State the preparation type.
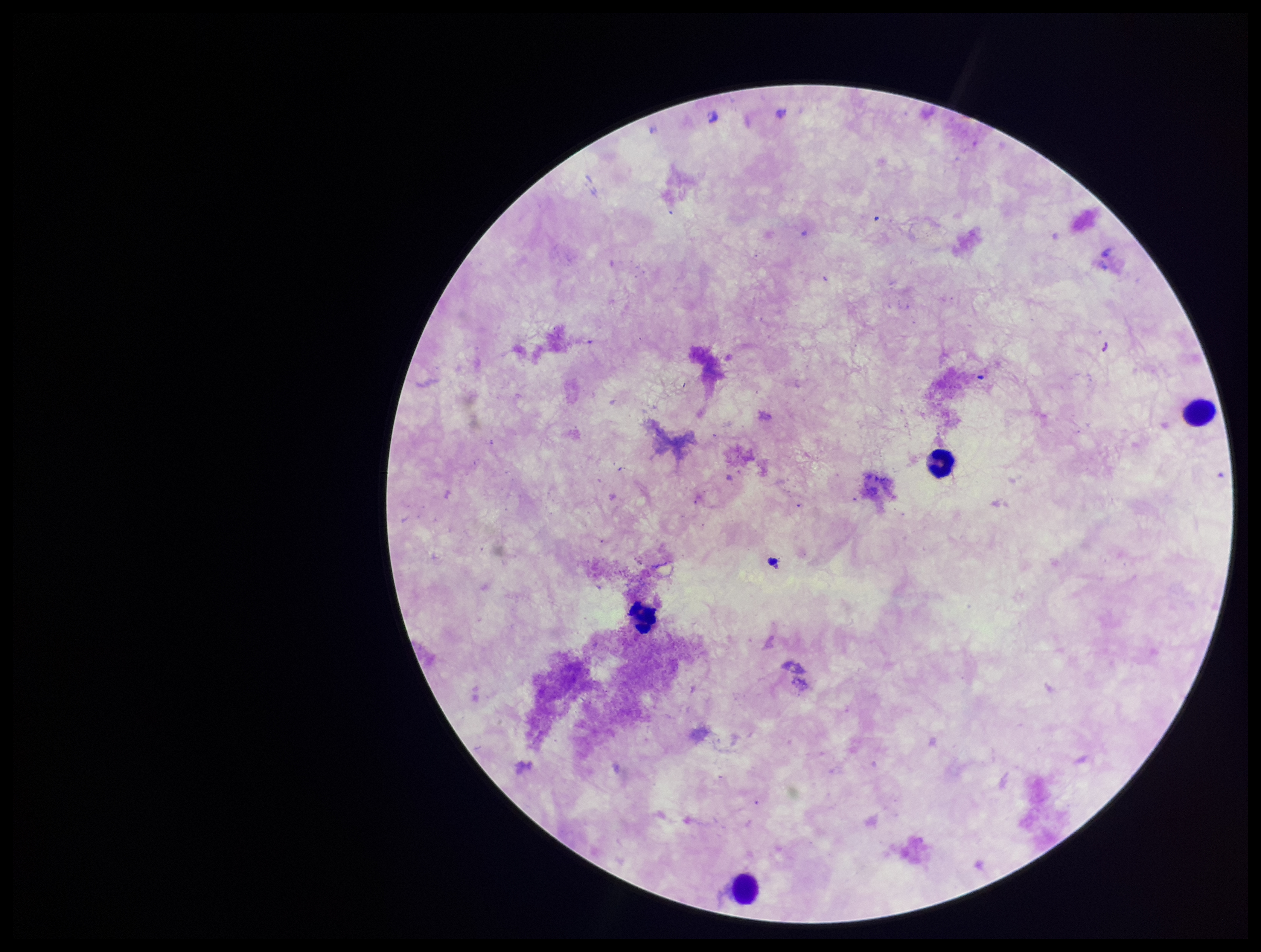

It is a thick blood smear.

Leukocyte count: 4. Giemsa stain. Patient malaria status: negative. Smartphone photograph taken through the eyepiece of a microscope. Parasite count: 0. Image is 1261×952 pixels. Plasmodium parasites: none detected. One field from this slide.